Assess this cell for malaria.
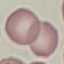
Uninfected.

Thin blood film. Cell patch, automatically extracted from a larger field of view and resized to 64 × 64 pixels. Giemsa-stained preparation. Acquired by smartphone through the microscope eyepiece.